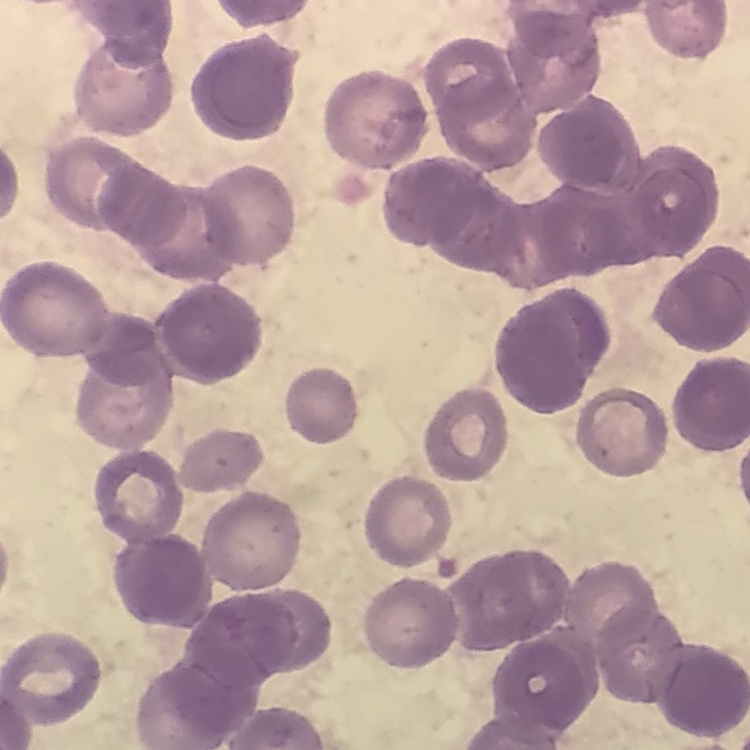 The red blood cells exhibit rouleaux formation. Stained with either Field's or Giemsa. Thin blood smear. Square crop of a larger photomicrograph.